Report the malaria status of this cell.
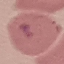

It is uninfected.

Giemsa stain. Photographed with a smartphone camera at the microscope eyepiece. Thin blood film. Cell patch, automatically extracted from a larger field of view and resized to 64 × 64 pixels.